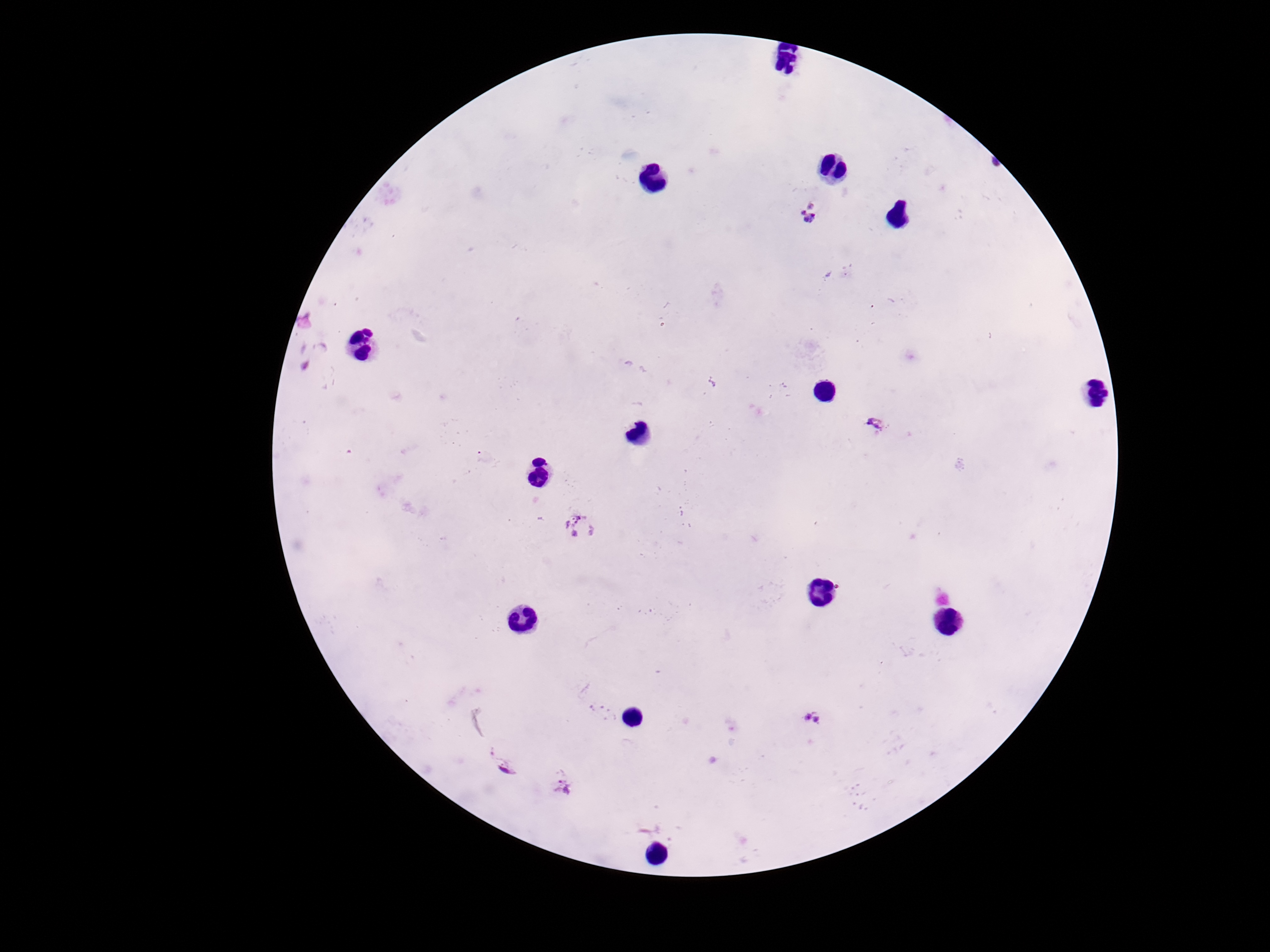 Approximate centers as (x, y) in pixels. Plasmodium parasite locations: (810, 217), (876, 428), (581, 529), (814, 718), (501, 764), (563, 785). Thick peripheral-blood smear. Photographed through the microscope eyepiece with a smartphone camera. Single field of view. Giemsa-stained preparation. Patient malaria status: positive. 100x magnification. Image is 1270×952 pixels.